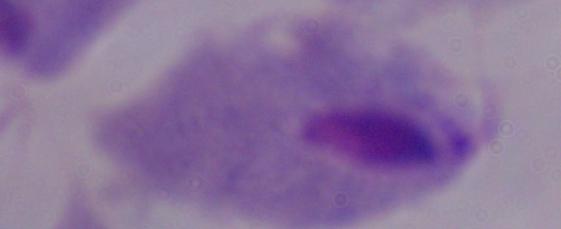

magnification: 1000x
modality: micrograph
identification: trichomonad